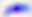

magnification: 400x
modality: micrograph
identification: Toxoplasma gondii